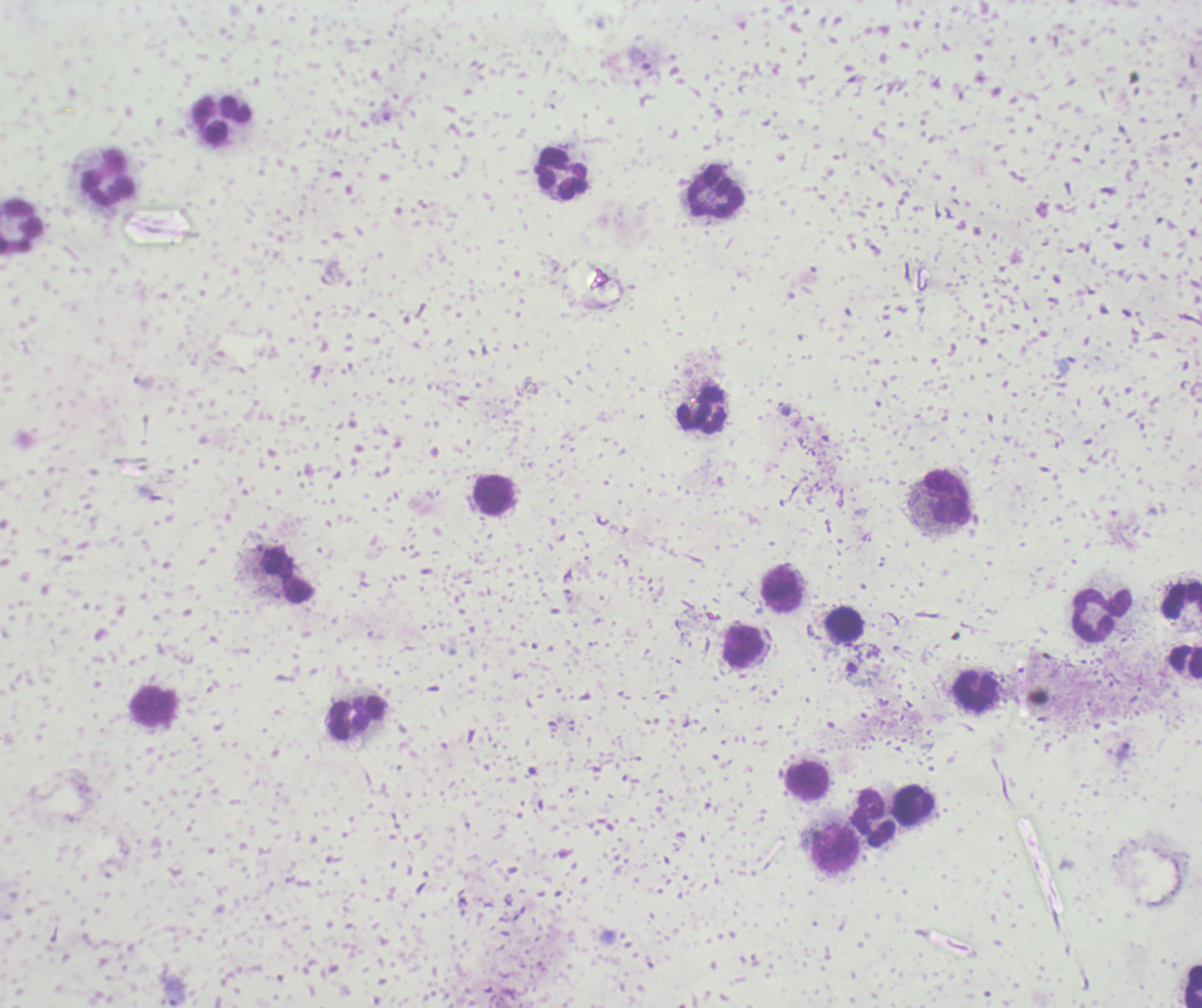

result: malaria parasites detected
image_size: 1202×1008 pixels
magnification: 100x
trophozoite_locations: 'approximate centers as (x, y) in pixels: (640, 60)'
stain: Romanowsky
field_of_view: one from this slide
leukocyte_locations: 'approximate centers as (x, y) in pixels: (222, 120), (559, 175), (109, 177), (715, 194), (22, 227), (701, 411), (494, 496), (948, 499), (285, 575), (782, 590), (1181, 599), (1101, 616), (845, 625), (743, 645), (1184, 660), (974, 690), (154, 706), (356, 718), (806, 782), (913, 805), (873, 817), (835, 850), (1193, 987)'
context: previously used in a real diagnosis
preparation: thick blood film
background_quality: poor